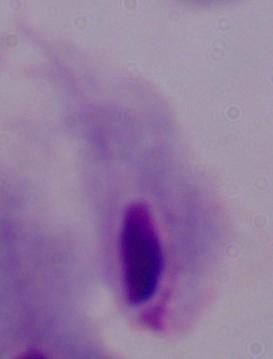

Summary:
  - Modality: micrograph
  - Identification: trichomonad
  - Magnification: 1000x